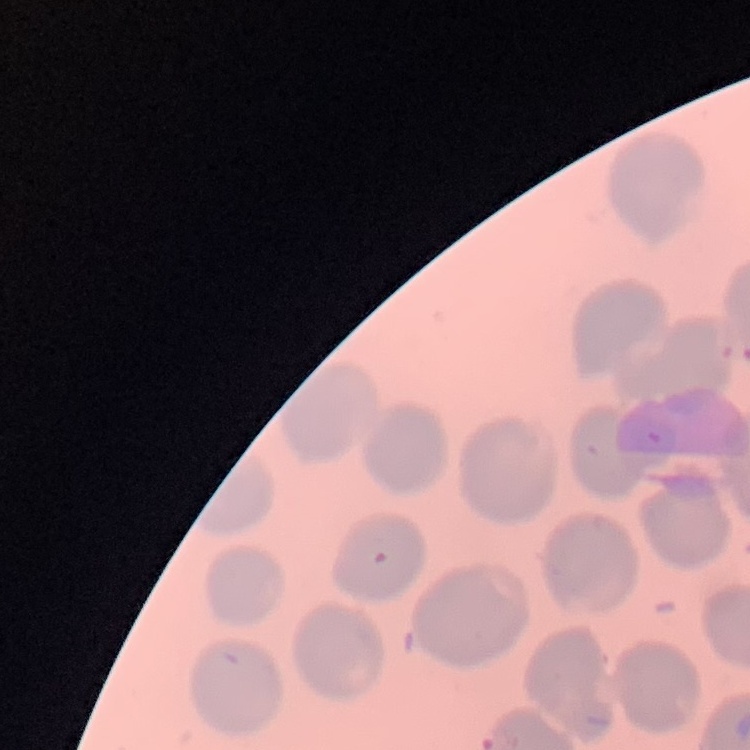

Summary:
  - Red blood cell morphology: no rouleaux formation
  - Preparation: thin peripheral smear
  - Stain: Field's or Giemsa
  - Image type: one tile cut from a larger photomicrograph